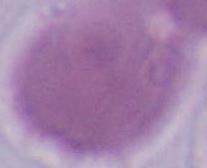
1000x magnification. Micrograph. An erythrocyte is shown.